Outline each blood parasite and name the species.
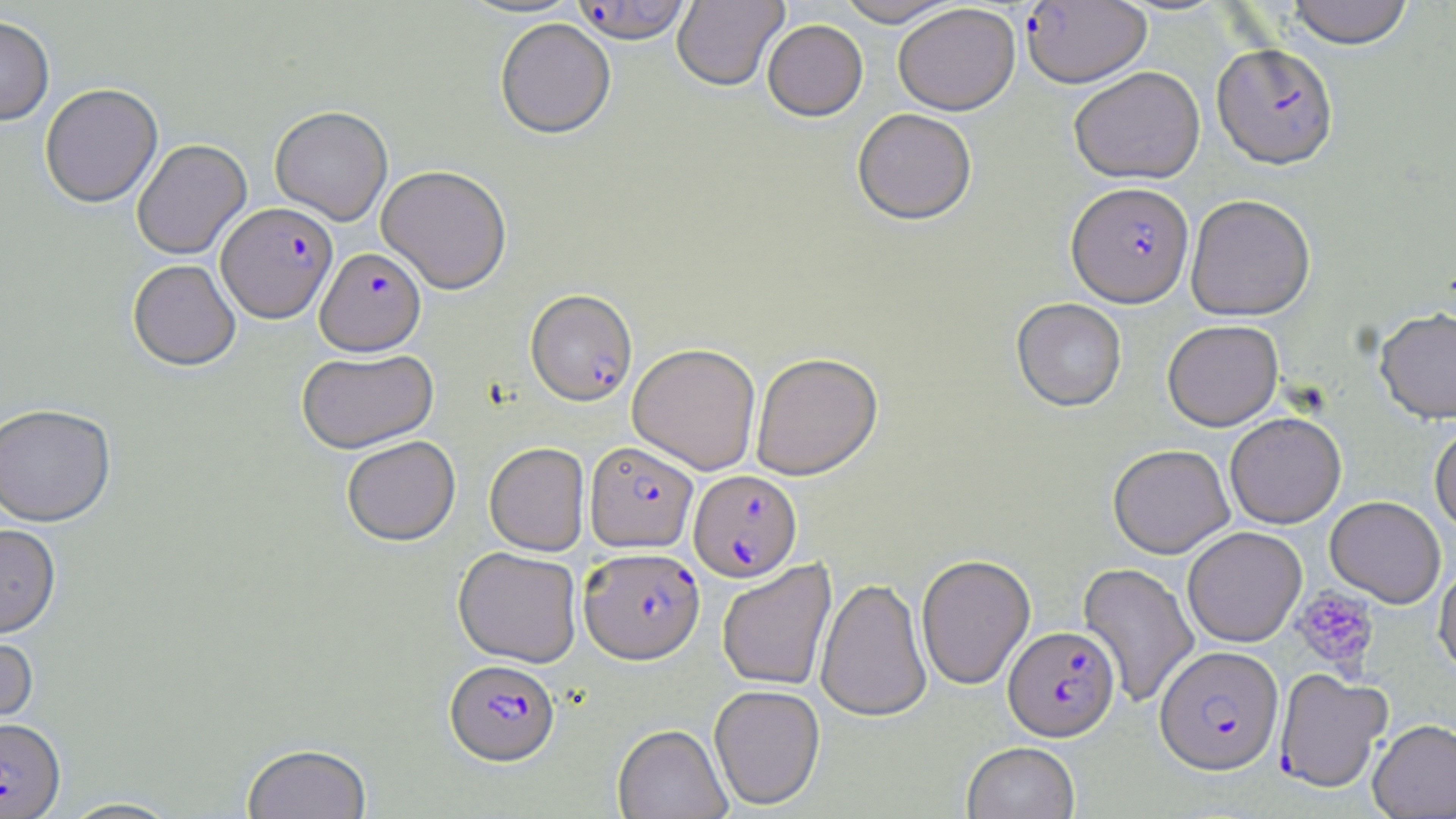

Approximate bounding boxes as (x1, y1, x2, y2) in pixels.
Plasmodium falciparum-infected red blood cells: (570, 1, 693, 46), (1021, 1, 1152, 87), (1212, 42, 1338, 168), (1067, 181, 1193, 306), (217, 202, 337, 323), (315, 247, 426, 356), (526, 289, 638, 406), (584, 441, 698, 553), (688, 469, 802, 582), (579, 547, 705, 664), (1004, 625, 1120, 741), (1155, 645, 1283, 775), (444, 659, 559, 767), (1274, 668, 1393, 793), (0, 717, 65, 818).
No Plasmodium ovale, Plasmodium malariae, Plasmodium vivax, Babesia divergens, or Trypanosoma brucei observed.

Summary:
  - Platelet locations: (1292, 587, 1379, 675)
  - Uninfected red blood cell locations: (672, 0, 788, 92), (834, 0, 962, 26), (1286, 0, 1414, 48), (893, 3, 1020, 115), (0, 15, 55, 125), (495, 19, 615, 139), (762, 19, 868, 121), (1069, 66, 1205, 184), (40, 83, 162, 208), (270, 105, 393, 225), (852, 108, 977, 225), (132, 139, 252, 260), (376, 164, 512, 294), (1185, 194, 1315, 320), (128, 258, 241, 371), (1011, 297, 1127, 412), (1375, 307, 1456, 423), (1162, 319, 1283, 431), (627, 342, 761, 475), (297, 348, 439, 454), (750, 351, 884, 480), (0, 403, 116, 527), (1225, 412, 1346, 528), (1430, 421, 1456, 533), (341, 435, 460, 546), (484, 442, 590, 556), (1108, 443, 1235, 558), (1325, 495, 1446, 608), (0, 524, 61, 639), (1182, 526, 1307, 647), (453, 546, 582, 667), (916, 553, 1036, 690), (1433, 557, 1456, 680), (717, 559, 837, 692), (1078, 561, 1200, 708), (816, 576, 932, 722), (0, 629, 39, 736), (709, 684, 825, 810), (1368, 719, 1456, 818), (612, 724, 732, 819), (962, 741, 1081, 819), (241, 742, 373, 819), (56, 797, 184, 818)
  - Slide-level diagnosis: Plasmodium falciparum
  - Magnification: 1000x
  - Modality: light microscopy
  - Preparation: thin blood smear
  - Field of view: single
  - Stain: May-Grünwald-Giemsa
  - Image size: 1456×819 pixels